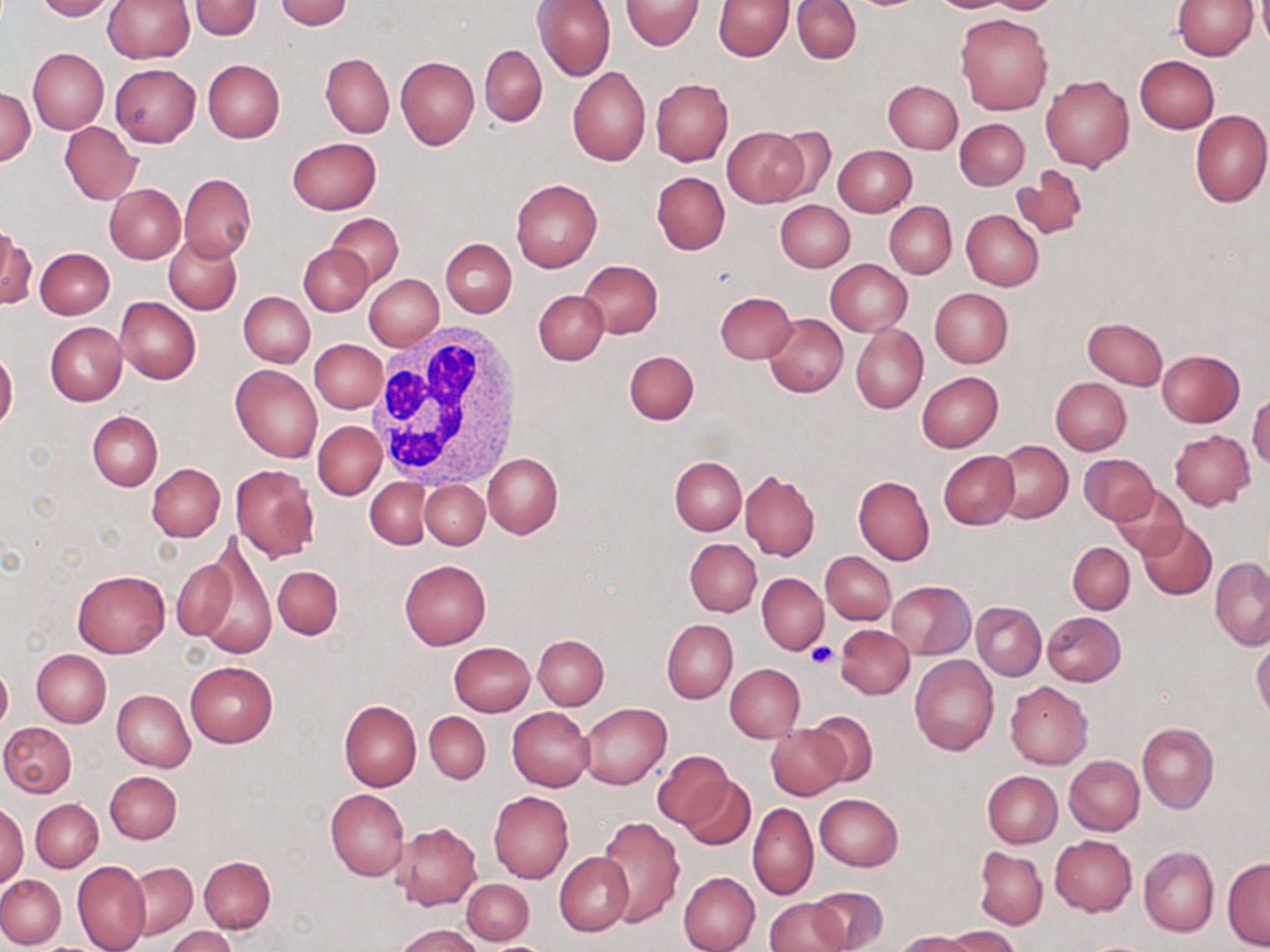
Approximate bounding boxes as (x1, y1, x2, y2) in pixels. Uninfected red blood cell locations: (31, 0, 116, 21), (103, 0, 193, 63), (276, 0, 353, 29), (534, 0, 616, 80), (712, 0, 794, 61), (792, 0, 862, 64), (929, 0, 1017, 13), (980, 0, 1063, 14), (1172, 0, 1258, 59), (620, 1, 703, 51), (189, 2, 262, 39), (955, 13, 1052, 115), (479, 44, 547, 127), (28, 49, 108, 133), (320, 53, 393, 137), (1134, 55, 1219, 132), (395, 56, 480, 148), (202, 59, 284, 142), (110, 63, 200, 146), (567, 67, 651, 165), (1040, 75, 1134, 171), (651, 78, 733, 166), (884, 80, 963, 152), (1, 88, 34, 166), (1190, 109, 1270, 208), (955, 119, 1028, 189), (60, 122, 141, 205), (722, 126, 808, 206), (767, 126, 838, 203), (288, 137, 381, 214), (833, 145, 916, 217), (1011, 166, 1088, 241), (652, 171, 731, 254), (177, 174, 256, 261), (511, 178, 602, 272), (105, 184, 185, 262), (776, 200, 855, 271), (885, 202, 955, 278), (961, 210, 1044, 290), (328, 214, 404, 287), (0, 226, 33, 311), (165, 236, 241, 315), (441, 238, 517, 317), (300, 245, 373, 315), (35, 247, 114, 318), (580, 260, 663, 338), (826, 260, 912, 336), (363, 274, 443, 350), (930, 288, 1013, 367), (534, 290, 609, 366), (715, 291, 797, 363), (239, 292, 314, 367), (116, 296, 200, 384), (764, 313, 848, 397), (1082, 317, 1167, 390), (45, 322, 127, 406), (851, 324, 927, 413), (310, 340, 386, 413), (1157, 349, 1245, 427), (625, 350, 699, 425), (0, 352, 18, 431), (230, 364, 322, 462), (916, 371, 1003, 452), (1051, 377, 1130, 455), (1248, 394, 1270, 468), (88, 410, 162, 491), (314, 421, 384, 500), (1169, 430, 1254, 509), (992, 439, 1072, 523), (939, 451, 1018, 530), (483, 453, 562, 538), (1079, 453, 1157, 524), (670, 456, 746, 535), (147, 464, 225, 540), (231, 464, 318, 561), (740, 469, 820, 561), (853, 476, 933, 565), (365, 479, 431, 548), (420, 480, 489, 548), (1110, 485, 1190, 560), (1138, 522, 1216, 599), (193, 538, 276, 661), (685, 538, 762, 616), (1067, 542, 1134, 614), (169, 552, 243, 648), (822, 552, 895, 624), (1211, 559, 1270, 651), (399, 560, 489, 649), (272, 565, 343, 640), (73, 569, 170, 657), (757, 573, 827, 654), (749, 576, 823, 726), (887, 580, 975, 659), (972, 602, 1046, 680), (1042, 611, 1126, 686), (662, 619, 738, 703), (836, 624, 914, 698), (534, 634, 608, 709), (1251, 640, 1270, 722), (449, 642, 535, 716), (32, 649, 112, 727), (911, 655, 999, 755), (185, 661, 278, 747), (0, 662, 12, 732), (725, 663, 805, 742), (1006, 681, 1093, 769), (112, 689, 195, 772), (339, 700, 422, 790), (580, 702, 671, 788), (507, 707, 595, 790), (806, 710, 879, 787), (425, 712, 490, 783), (2, 722, 76, 797), (1138, 722, 1217, 814), (767, 723, 849, 799), (652, 751, 733, 829), (1064, 755, 1144, 835), (105, 770, 182, 844), (982, 770, 1061, 848), (681, 775, 754, 850), (326, 788, 409, 881), (489, 791, 573, 883), (815, 793, 903, 871), (31, 799, 103, 872), (0, 802, 28, 889), (748, 803, 818, 901), (597, 817, 685, 927), (391, 821, 483, 911), (1049, 835, 1136, 916), (974, 846, 1047, 929), (1139, 846, 1218, 938), (554, 852, 633, 935), (199, 856, 275, 933), (73, 859, 150, 952), (1222, 859, 1270, 950), (128, 862, 197, 939), (678, 871, 760, 952), (0, 875, 66, 949), (461, 878, 535, 944), (809, 886, 888, 950), (765, 899, 849, 952), (396, 923, 483, 952), (167, 926, 235, 952), (944, 927, 1021, 951), (897, 931, 979, 952), (1083, 940, 1154, 952). White blood cell locations: (368, 325, 527, 488). Platelet locations: (807, 643, 838, 667). Slide-level diagnosis: negative for blood parasites. Optical microscopy. 1000x magnification. May-Grünwald-Giemsa stain. Thin blood smear. Image is 1270×952 pixels. Single field of view.